Report the malaria status of this cell.
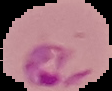

It is parasitized.

Summary:
  - Image size: 112×91 pixels
  - Preparation: thin blood smear
  - Image type: cell region segmented out of the field of view; surrounding area masked to black